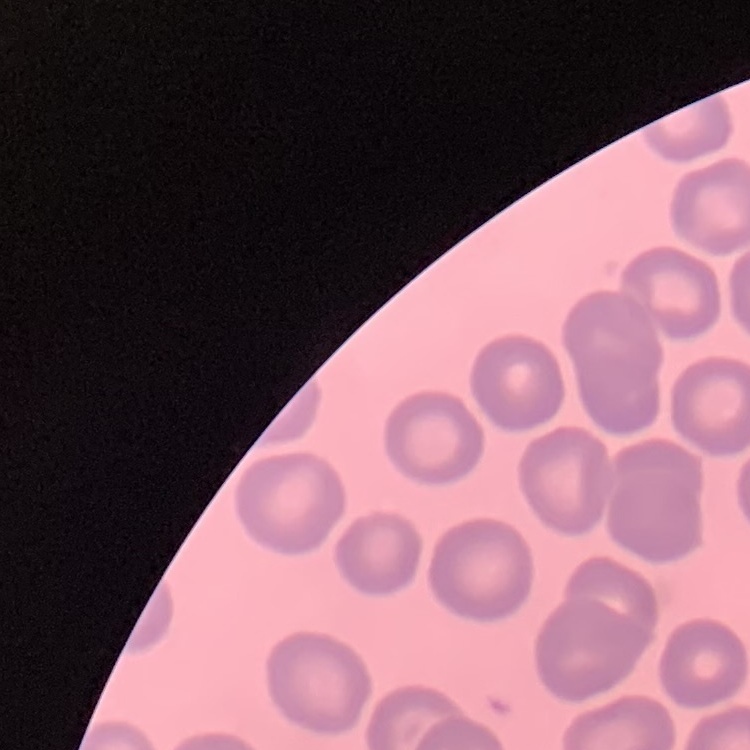 The erythrocytes show no rouleaux formation. One tile cut from a larger photomicrograph. Field's or Giemsa stain. Thin peripheral smear.